Name the parasite shown.
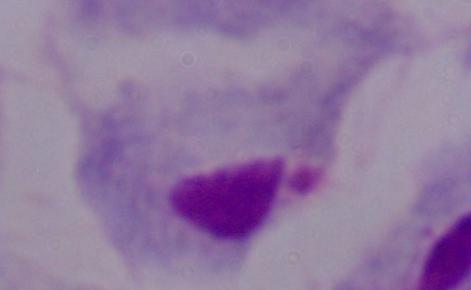

A trichomonad.

Summary:
  - Modality: photomicrograph
  - Magnification: 1000x